Identify the parasite.
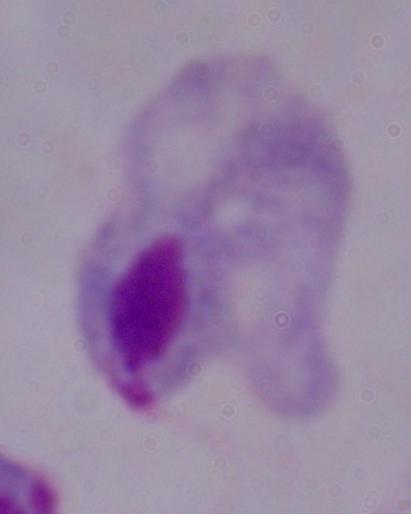
A trichomonad.

{
  "magnification": "1000x",
  "modality": "photomicrograph"
}